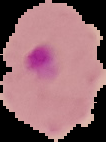 Image is 106×142 pixels. From a thin blood smear. Segmented cell region on a black background. Malaria status: parasitized.